State which cell type is depicted.
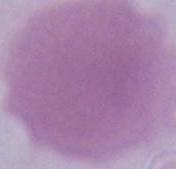

This is an erythrocyte.

modality: micrograph
magnification: 1000x